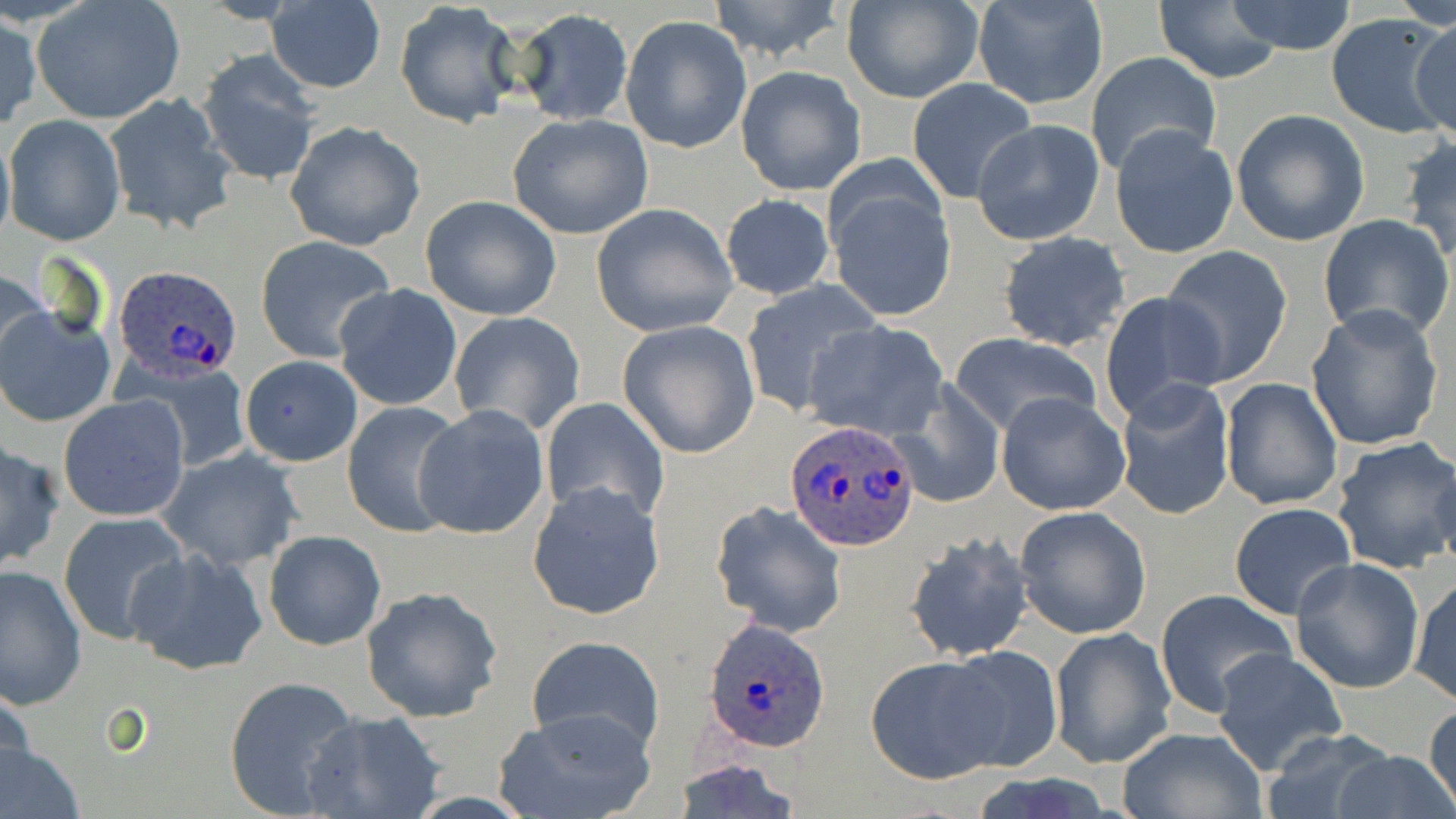

{
  "slide_level_diagnosis": "Plasmodium ovale",
  "uninfected_red_blood_cell_locations": "approximate bounding boxes as named x1/y1/x2/y2 corners in pixels: (x1=706, y1=0, x2=851, y2=63), (x1=1222, y1=0, x2=1361, y2=55), (x1=33, y1=1, x2=187, y2=125), (x1=841, y1=1, x2=983, y2=104), (x1=971, y1=2, x2=1107, y2=110), (x1=1153, y1=2, x2=1286, y2=84), (x1=264, y1=3, x2=386, y2=92), (x1=394, y1=4, x2=520, y2=129), (x1=509, y1=8, x2=634, y2=125), (x1=1325, y1=11, x2=1455, y2=140), (x1=1, y1=12, x2=41, y2=132), (x1=1411, y1=12, x2=1456, y2=140), (x1=620, y1=15, x2=752, y2=155), (x1=195, y1=50, x2=322, y2=186), (x1=1085, y1=52, x2=1222, y2=177), (x1=735, y1=66, x2=866, y2=196), (x1=906, y1=77, x2=1036, y2=203), (x1=103, y1=93, x2=238, y2=235), (x1=1230, y1=108, x2=1369, y2=246), (x1=507, y1=113, x2=654, y2=241), (x1=4, y1=114, x2=125, y2=245), (x1=0, y1=120, x2=15, y2=250), (x1=285, y1=120, x2=426, y2=251), (x1=973, y1=120, x2=1106, y2=247), (x1=1109, y1=124, x2=1238, y2=260), (x1=1402, y1=137, x2=1456, y2=264), (x1=824, y1=169, x2=958, y2=324), (x1=719, y1=193, x2=836, y2=301), (x1=420, y1=194, x2=564, y2=321), (x1=590, y1=203, x2=738, y2=337), (x1=1318, y1=213, x2=1454, y2=344), (x1=997, y1=232, x2=1131, y2=352), (x1=254, y1=235, x2=396, y2=362), (x1=1159, y1=248, x2=1293, y2=385), (x1=0, y1=268, x2=53, y2=385), (x1=738, y1=281, x2=884, y2=419), (x1=333, y1=284, x2=464, y2=412), (x1=1099, y1=290, x2=1226, y2=424), (x1=0, y1=305, x2=114, y2=428), (x1=1303, y1=305, x2=1445, y2=451), (x1=449, y1=311, x2=586, y2=436), (x1=801, y1=320, x2=949, y2=442), (x1=617, y1=321, x2=761, y2=458), (x1=949, y1=330, x2=1103, y2=439), (x1=238, y1=355, x2=363, y2=467), (x1=148, y1=364, x2=252, y2=472), (x1=1219, y1=376, x2=1344, y2=508), (x1=1114, y1=377, x2=1235, y2=521), (x1=890, y1=378, x2=1008, y2=508), (x1=996, y1=390, x2=1131, y2=515), (x1=59, y1=395, x2=189, y2=522), (x1=541, y1=397, x2=669, y2=526), (x1=343, y1=401, x2=469, y2=540), (x1=412, y1=404, x2=551, y2=540), (x1=1330, y1=436, x2=1456, y2=575), (x1=0, y1=440, x2=64, y2=573), (x1=1431, y1=447, x2=1454, y2=573), (x1=157, y1=448, x2=304, y2=571), (x1=527, y1=482, x2=665, y2=622), (x1=711, y1=501, x2=847, y2=637), (x1=1229, y1=501, x2=1357, y2=619), (x1=1014, y1=507, x2=1151, y2=638), (x1=58, y1=512, x2=192, y2=648), (x1=263, y1=529, x2=387, y2=651), (x1=904, y1=532, x2=1035, y2=662), (x1=124, y1=547, x2=268, y2=674), (x1=1291, y1=555, x2=1425, y2=694), (x1=0, y1=566, x2=87, y2=709), (x1=1408, y1=576, x2=1455, y2=708), (x1=361, y1=586, x2=503, y2=723), (x1=1155, y1=588, x2=1296, y2=719), (x1=1048, y1=627, x2=1177, y2=768), (x1=526, y1=635, x2=664, y2=756), (x1=936, y1=645, x2=1065, y2=773), (x1=1210, y1=648, x2=1347, y2=775), (x1=864, y1=656, x2=1008, y2=782), (x1=223, y1=674, x2=360, y2=818), (x1=1, y1=678, x2=36, y2=802), (x1=1425, y1=702, x2=1456, y2=816), (x1=495, y1=706, x2=655, y2=819), (x1=300, y1=710, x2=446, y2=819), (x1=1115, y1=725, x2=1268, y2=818), (x1=1260, y1=729, x2=1399, y2=819), (x1=0, y1=738, x2=84, y2=819), (x1=1334, y1=748, x2=1453, y2=819), (x1=668, y1=759, x2=808, y2=819)",
  "stain": "May-Grünwald-Giemsa",
  "image_size": "1456×819 pixels",
  "preparation": "thin blood film",
  "modality": "light microscopy",
  "plasmodium_ovale_infected_red_blood_cell_locations": "approximate bounding boxes as named x1/y1/x2/y2 corners in pixels: (x1=110, y1=265, x2=245, y2=387), (x1=785, y1=420, x2=920, y2=551), (x1=701, y1=617, x2=832, y2=754)",
  "field_of_view": "single",
  "magnification": "1000x"
}